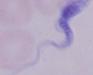

A trypanosome is seen. 1000x magnification. Micrograph.